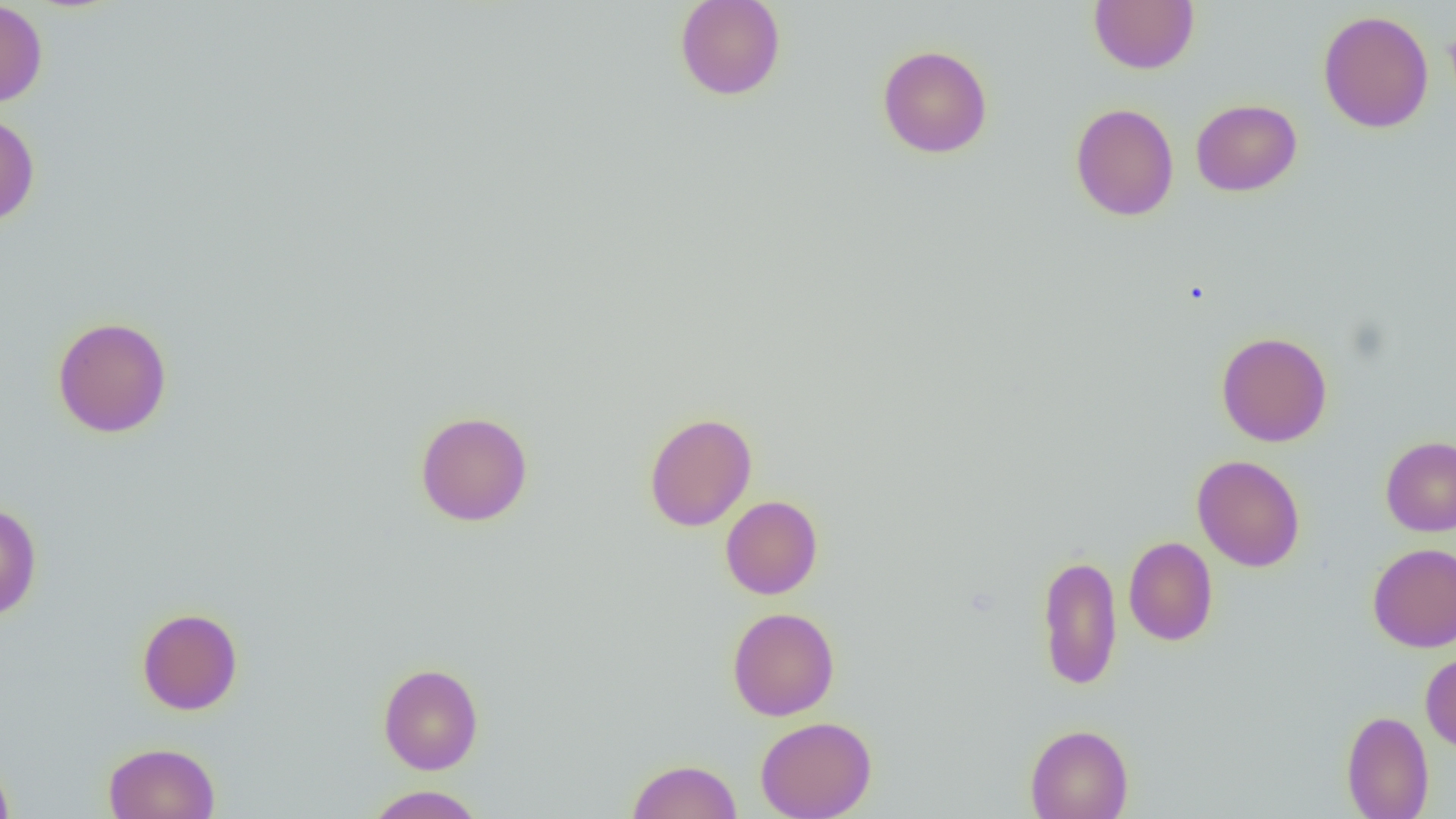
slide-level diagnosis = negative for blood parasites
image size = 1456×819 pixels
modality = optical microscopy
uninfected red blood cell locations = approximate bounding boxes as [x1, y1, x2, y2] in pixels: [675, 0, 786, 100], [0, 1, 48, 108], [1089, 1, 1199, 73], [1318, 10, 1433, 133], [877, 44, 992, 158], [1191, 99, 1302, 196], [1070, 103, 1178, 221], [0, 111, 40, 227], [52, 316, 173, 438], [1216, 331, 1332, 447], [415, 410, 533, 527], [644, 412, 757, 532], [1380, 436, 1456, 536], [1192, 454, 1305, 571], [720, 495, 823, 600], [0, 502, 42, 621], [1123, 537, 1218, 646], [1368, 542, 1456, 652], [1036, 553, 1122, 692], [137, 607, 243, 715], [727, 607, 840, 721], [1420, 650, 1456, 754], [378, 663, 484, 774], [1341, 709, 1434, 819], [755, 716, 877, 819], [1024, 724, 1134, 819], [103, 741, 220, 819], [0, 753, 16, 819], [626, 759, 742, 819], [363, 785, 487, 818]
magnification = 1000x
field of view = one of a larger specimen
preparation = thin blood smear